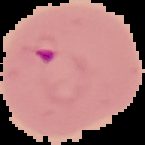
Malaria status: parasitized. Cell region segmented out of the field of view; the surrounding area is masked to black. From a thin blood smear. Image is 145×145 pixels.